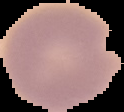

Summary:
  - Result: negative for Plasmodium parasites
  - Image type: cell region segmented out of the field of view; surrounding area masked to black
  - Image size: 124×112 pixels
  - Preparation: thin blood smear